Identify the parasite.
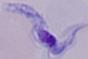

A trypanosome.

1000x magnification. Photomicrograph.